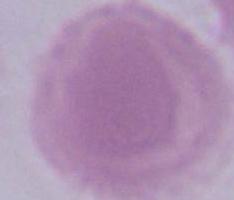
Summary:
  - Magnification: 1000x
  - Identification: red blood cell
  - Modality: photomicrograph